Identify the cell.
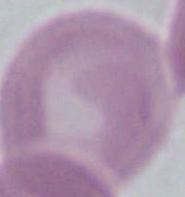

This is an erythrocyte.

Summary:
  - Modality: micrograph
  - Magnification: 1000x